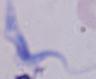
Summary:
  - Magnification: 1000x
  - Modality: photomicrograph
  - Identification: trypanosome